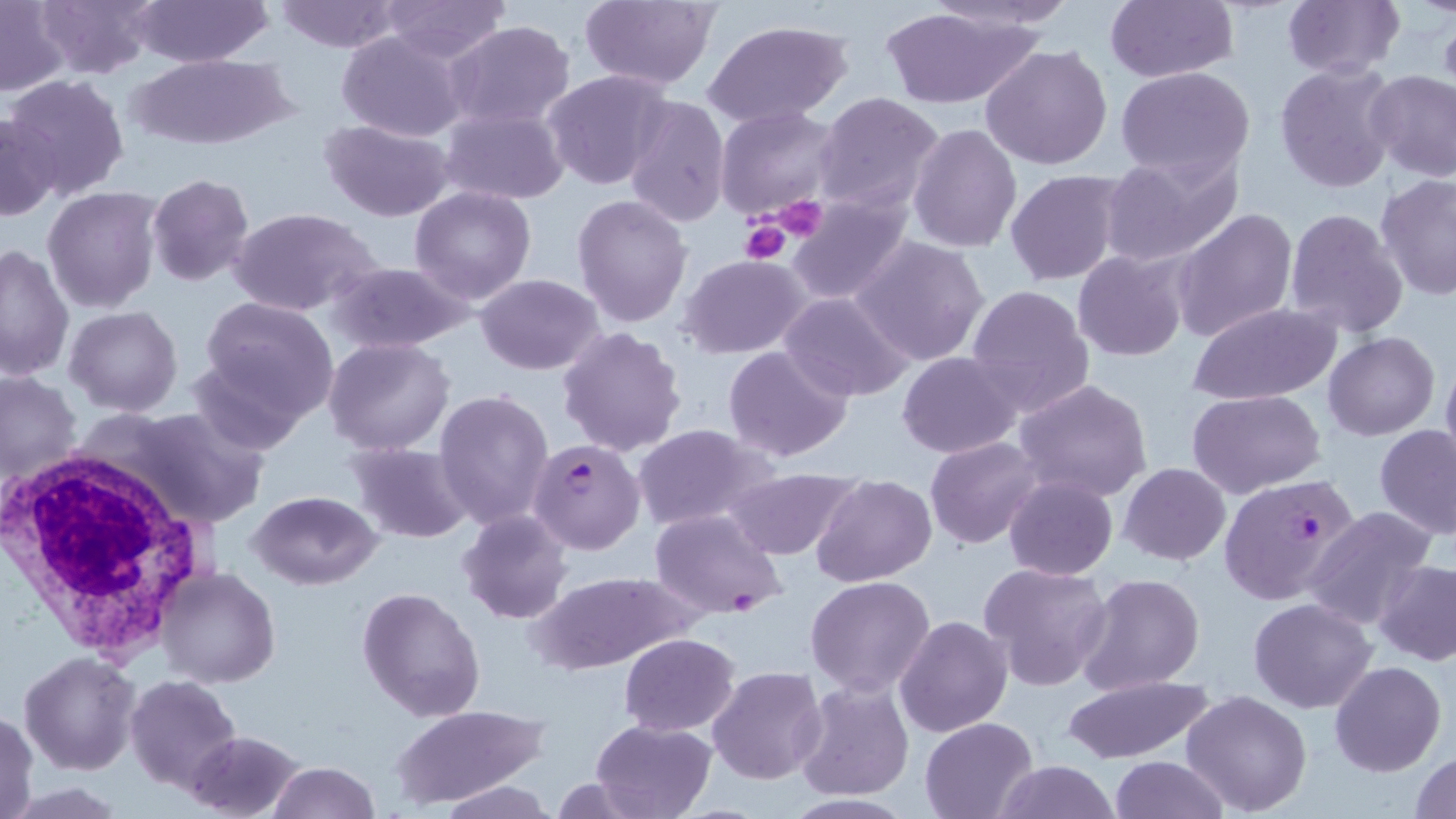

slide-level diagnosis = Plasmodium falciparum
platelet locations = approximate bounding boxes as named x1/y1/x2/y2 corners in pixels: (x1=767, y1=196, x2=830, y2=242), (x1=739, y1=220, x2=792, y2=266)
image size = 1456×819 pixels
uninfected red blood cell locations = approximate bounding boxes as named x1/y1/x2/y2 corners in pixels: (x1=35, y1=0, x2=156, y2=80), (x1=274, y1=0, x2=403, y2=52), (x1=381, y1=0, x2=510, y2=63), (x1=576, y1=0, x2=720, y2=90), (x1=1106, y1=0, x2=1239, y2=83), (x1=1280, y1=0, x2=1404, y2=81), (x1=131, y1=1, x2=273, y2=67), (x1=0, y1=2, x2=68, y2=95), (x1=880, y1=5, x2=1045, y2=110), (x1=445, y1=21, x2=577, y2=131), (x1=703, y1=21, x2=850, y2=129), (x1=335, y1=30, x2=468, y2=143), (x1=981, y1=44, x2=1114, y2=170), (x1=128, y1=54, x2=290, y2=148), (x1=1274, y1=62, x2=1400, y2=194), (x1=1115, y1=66, x2=1257, y2=182), (x1=1366, y1=69, x2=1456, y2=182), (x1=543, y1=70, x2=672, y2=189), (x1=4, y1=75, x2=130, y2=199), (x1=812, y1=92, x2=945, y2=214), (x1=624, y1=94, x2=732, y2=228), (x1=717, y1=106, x2=842, y2=220), (x1=439, y1=108, x2=569, y2=203), (x1=1, y1=114, x2=61, y2=220), (x1=320, y1=118, x2=454, y2=221), (x1=907, y1=124, x2=1022, y2=253), (x1=1099, y1=149, x2=1245, y2=268), (x1=1004, y1=170, x2=1125, y2=284), (x1=1374, y1=173, x2=1456, y2=302), (x1=146, y1=174, x2=255, y2=286), (x1=409, y1=185, x2=537, y2=304), (x1=43, y1=187, x2=165, y2=313), (x1=788, y1=193, x2=912, y2=304), (x1=571, y1=195, x2=693, y2=328), (x1=229, y1=207, x2=382, y2=316), (x1=1172, y1=208, x2=1297, y2=341), (x1=1283, y1=208, x2=1407, y2=339), (x1=848, y1=235, x2=992, y2=366), (x1=0, y1=243, x2=74, y2=380), (x1=1074, y1=251, x2=1190, y2=361), (x1=681, y1=255, x2=810, y2=358), (x1=325, y1=260, x2=475, y2=356), (x1=476, y1=274, x2=604, y2=375), (x1=965, y1=284, x2=1096, y2=416), (x1=780, y1=292, x2=913, y2=403), (x1=201, y1=297, x2=338, y2=419), (x1=1186, y1=302, x2=1342, y2=405), (x1=63, y1=305, x2=182, y2=417), (x1=558, y1=326, x2=688, y2=456), (x1=1322, y1=332, x2=1439, y2=441), (x1=323, y1=339, x2=455, y2=454), (x1=722, y1=343, x2=854, y2=463), (x1=188, y1=349, x2=310, y2=457), (x1=896, y1=352, x2=1021, y2=458), (x1=1440, y1=352, x2=1456, y2=476), (x1=1, y1=369, x2=82, y2=485), (x1=1014, y1=379, x2=1153, y2=502), (x1=435, y1=389, x2=556, y2=529), (x1=1187, y1=389, x2=1325, y2=498), (x1=121, y1=406, x2=269, y2=528), (x1=1375, y1=424, x2=1455, y2=539), (x1=631, y1=425, x2=776, y2=531), (x1=925, y1=437, x2=1044, y2=550), (x1=346, y1=441, x2=473, y2=544), (x1=1119, y1=464, x2=1230, y2=564), (x1=721, y1=467, x2=859, y2=560), (x1=811, y1=474, x2=935, y2=587), (x1=1004, y1=474, x2=1118, y2=581), (x1=247, y1=491, x2=383, y2=589), (x1=1302, y1=507, x2=1436, y2=628), (x1=457, y1=508, x2=572, y2=625), (x1=1373, y1=559, x2=1456, y2=665), (x1=977, y1=561, x2=1113, y2=690), (x1=155, y1=567, x2=279, y2=689), (x1=528, y1=571, x2=692, y2=674), (x1=1077, y1=574, x2=1205, y2=696), (x1=805, y1=575, x2=936, y2=697), (x1=358, y1=586, x2=486, y2=723), (x1=1249, y1=598, x2=1377, y2=714), (x1=895, y1=614, x2=1013, y2=738), (x1=619, y1=633, x2=739, y2=735), (x1=19, y1=652, x2=141, y2=774), (x1=1329, y1=661, x2=1445, y2=776), (x1=707, y1=666, x2=828, y2=784), (x1=1060, y1=672, x2=1213, y2=764), (x1=123, y1=675, x2=243, y2=793), (x1=794, y1=676, x2=914, y2=800), (x1=1181, y1=690, x2=1313, y2=815), (x1=390, y1=704, x2=549, y2=808), (x1=1, y1=709, x2=40, y2=819), (x1=918, y1=717, x2=1038, y2=819), (x1=590, y1=718, x2=715, y2=819), (x1=184, y1=729, x2=306, y2=818), (x1=1409, y1=751, x2=1454, y2=818), (x1=1109, y1=755, x2=1228, y2=818), (x1=992, y1=759, x2=1121, y2=819), (x1=268, y1=762, x2=380, y2=818), (x1=437, y1=781, x2=556, y2=817)
field of view = single
magnification = 1000x
preparation = thin blood smear
white blood cell locations = approximate bounding boxes as named x1/y1/x2/y2 corners in pixels: (x1=0, y1=437, x2=220, y2=662)
stain = May-Grünwald-Giemsa
modality = light microscopy
Plasmodium falciparum-infected red blood cell locations = approximate bounding boxes as named x1/y1/x2/y2 corners in pixels: (x1=530, y1=438, x2=646, y2=554), (x1=1218, y1=474, x2=1361, y2=606), (x1=649, y1=508, x2=787, y2=618)